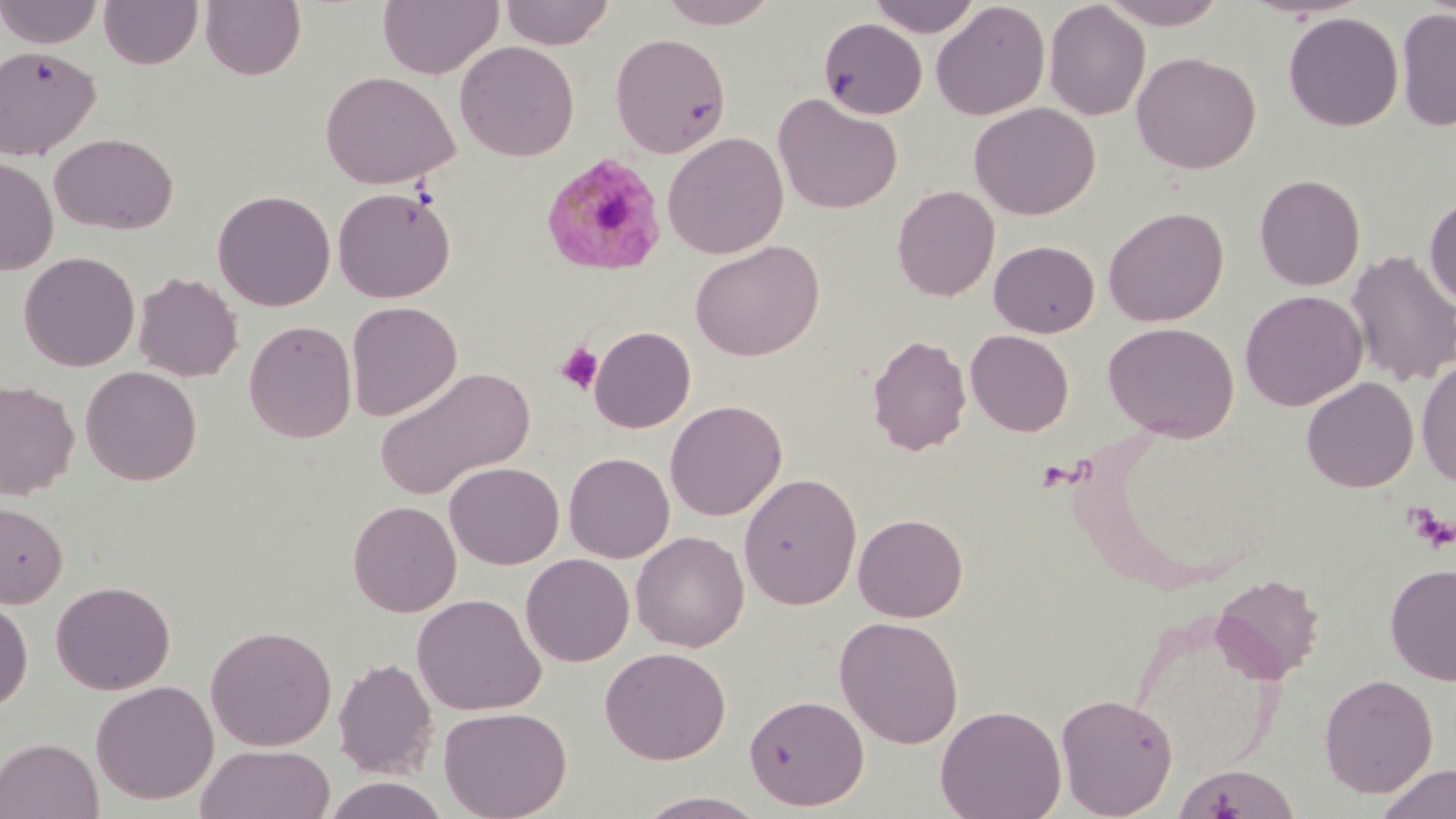

Approximate bounding boxes as (x1,y1)-(x2,y2) corner pairs in pixels. Uninfected red blood cell locations: (0,0)-(104,48), (200,0)-(307,81), (377,0)-(503,79), (499,0)-(615,49), (657,0)-(781,28), (867,0)-(982,37), (1099,0)-(1230,29), (98,1)-(203,69), (931,1)-(1051,121), (1043,1)-(1151,121), (1395,7)-(1456,132), (1283,11)-(1403,131), (818,17)-(928,120), (609,32)-(731,158), (455,41)-(580,162), (0,45)-(101,160), (1131,51)-(1261,174), (320,70)-(460,190), (772,93)-(903,214), (969,102)-(1100,220), (49,132)-(178,235), (663,132)-(788,259), (0,156)-(59,276), (1254,174)-(1365,290), (891,185)-(1000,302), (332,186)-(457,304), (212,189)-(336,311), (1423,193)-(1456,311), (1103,206)-(1229,326), (689,240)-(825,362), (989,240)-(1100,337), (1345,249)-(1456,387), (19,252)-(140,372), (132,271)-(243,382), (1240,289)-(1368,411), (345,300)-(462,422), (244,319)-(357,443), (1102,321)-(1240,442), (589,326)-(696,433), (965,329)-(1074,436), (867,334)-(971,457), (1416,359)-(1456,487), (80,366)-(202,485), (374,366)-(534,500), (1301,376)-(1419,492), (0,379)-(79,500), (665,399)-(787,521), (563,452)-(674,563), (445,461)-(564,569), (738,472)-(862,610), (0,500)-(68,609), (347,500)-(462,617), (853,513)-(968,622), (631,531)-(749,653), (520,553)-(635,667), (1385,563)-(1456,686), (1211,573)-(1324,683), (51,580)-(175,695), (411,593)-(546,716), (0,595)-(33,711), (1128,610)-(1287,779), (834,615)-(964,748), (205,624)-(336,751), (600,646)-(731,764), (332,657)-(438,779), (1319,673)-(1438,797), (90,680)-(219,805), (1055,692)-(1179,818), (743,693)-(869,811), (935,704)-(1066,819), (438,705)-(572,819), (0,737)-(103,819), (195,744)-(335,819), (1173,763)-(1300,819), (1377,763)-(1456,819), (322,776)-(450,819), (635,790)-(770,818). Plasmodium malariae-infected red blood cell locations: (540,151)-(668,276). Platelet locations: (555,341)-(603,394), (1409,507)-(1455,552). Slide-level diagnosis: Plasmodium malariae. Light microscopy. Image is 1456×819 pixels. Thin blood smear. Captured at 1000x magnification. May-Grünwald-Giemsa stain. Single field of view.